Name the cell type shown.
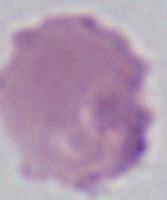

An erythrocyte.

Summary:
  - Magnification: 1000x
  - Modality: micrograph